Comment on the morphology of the erythrocytes.
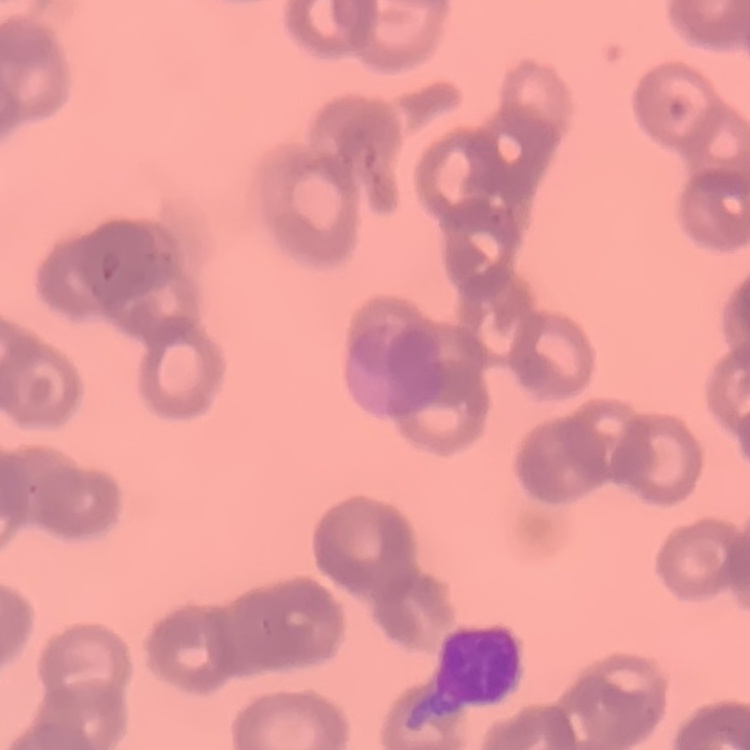
Rouleaux formation.

Summary:
  - Preparation: thin peripheral smear
  - Stain: Field's or Giemsa
  - Image type: square crop of a larger photomicrograph